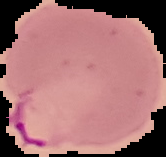
Cell region segmented out of the field of view; the surrounding area is masked to black. From a thin blood smear. Image is 166×157 pixels. Malaria status: parasitized.